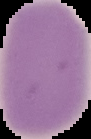

Summary:
  - Image type: cell region segmented out of the field of view; surrounding area masked to black
  - Image size: 91×139 pixels
  - Preparation: thin blood smear
  - Malaria status: uninfected